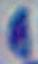
{
  "modality": "micrograph",
  "identification": "Toxoplasma gondii",
  "magnification": "1000x"
}